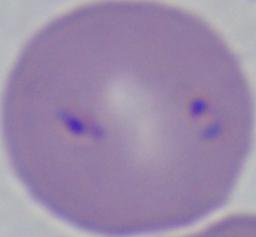
Summary:
  - Identification: Babesia
  - Modality: photomicrograph
  - Magnification: 1000x